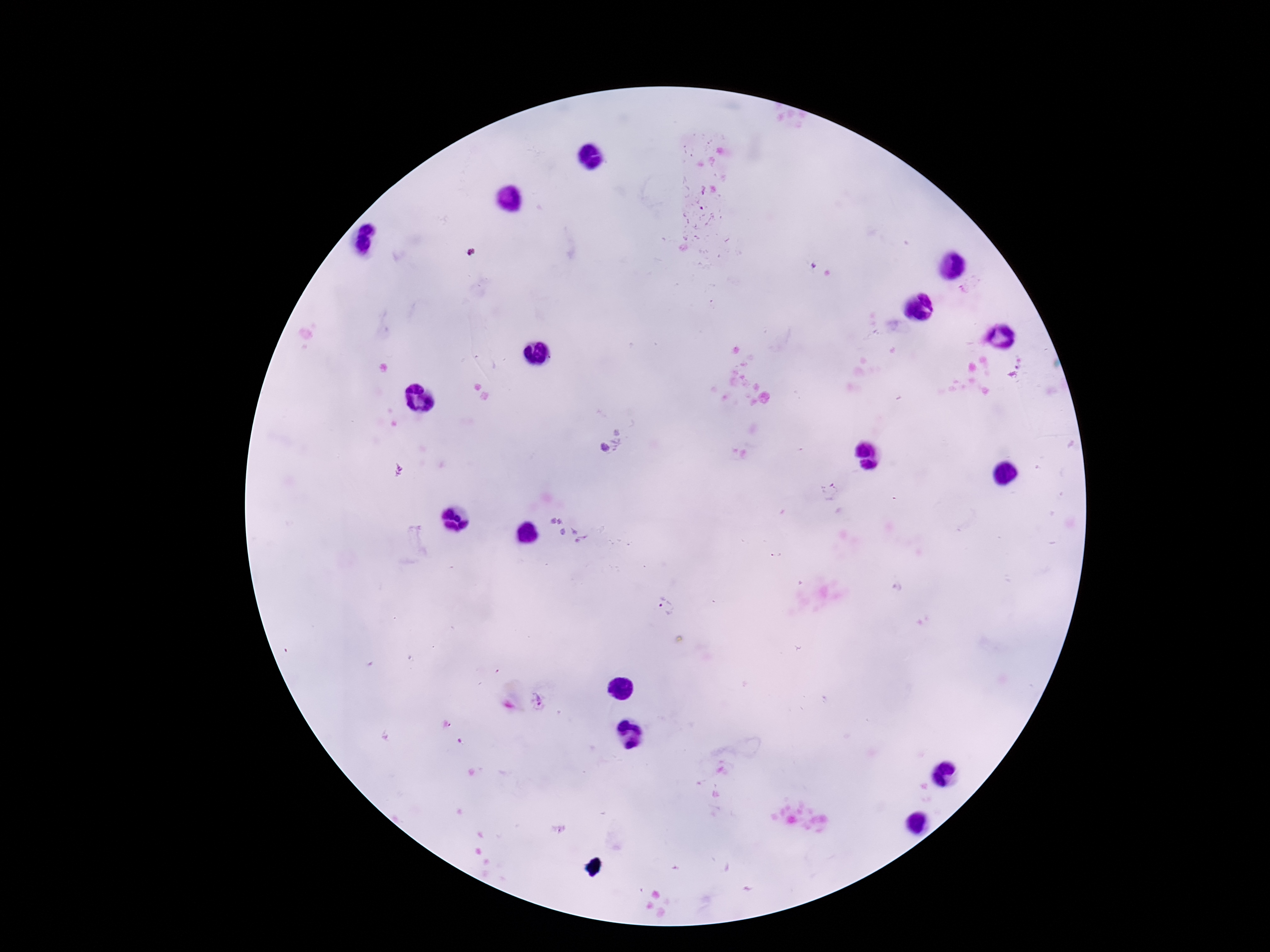

Approximate object centers, in pixels from the top-left corner.
Summary:
  - Plasmodium parasite locations: (x=622, y=437), (x=603, y=447), (x=830, y=492), (x=666, y=605), (x=541, y=701)
  - Magnification: 100x
  - Capture: smartphone camera through the microscope eyepiece
  - Preparation: thick peripheral-blood smear
  - Stain: Giemsa
  - Field of view: one from this slide
  - Patient malaria status: infected
  - Image size: 1270×952 pixels